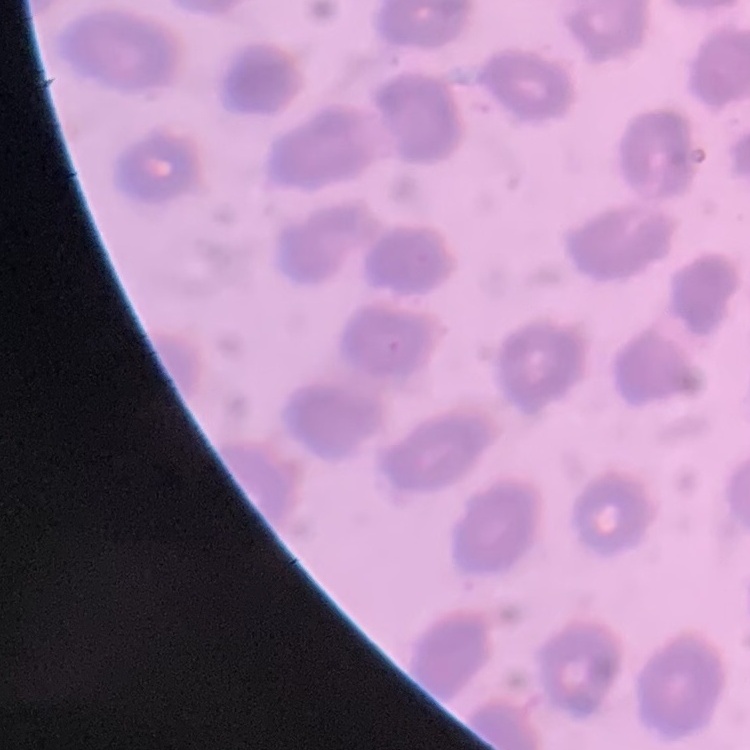

{
  "erythrocyte_morphology": "no rouleaux formation",
  "image_type": "one tile cut from a larger photomicrograph",
  "preparation": "thin blood film",
  "stain": "Field's or Giemsa"
}